Report the malaria status of this cell.
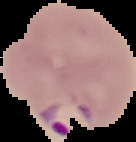
Parasitized.

Summary:
  - Image type: cell region segmented out of the field of view; surrounding area masked to black
  - Preparation: thin blood film
  - Image size: 136×142 pixels